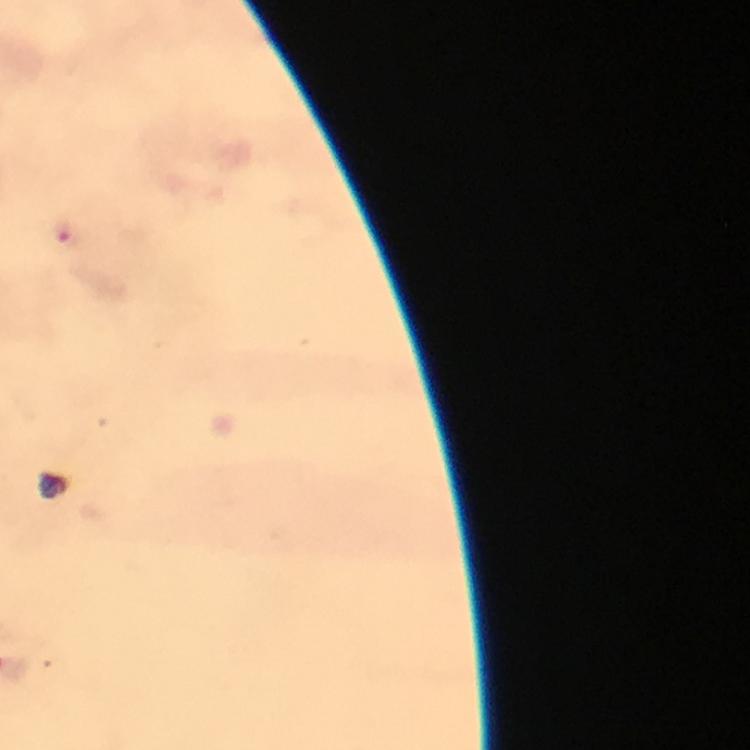
Approximate centers as (x, y) in pixels. Malaria parasite locations: (63, 232). Immersion oil was used. Giemsa stain. From a diagnostic examination for malaria. At 100x magnification. A crop from one field of view. Image is 750×750 pixels. Thick blood film. Smartphone photograph taken through a microscope.